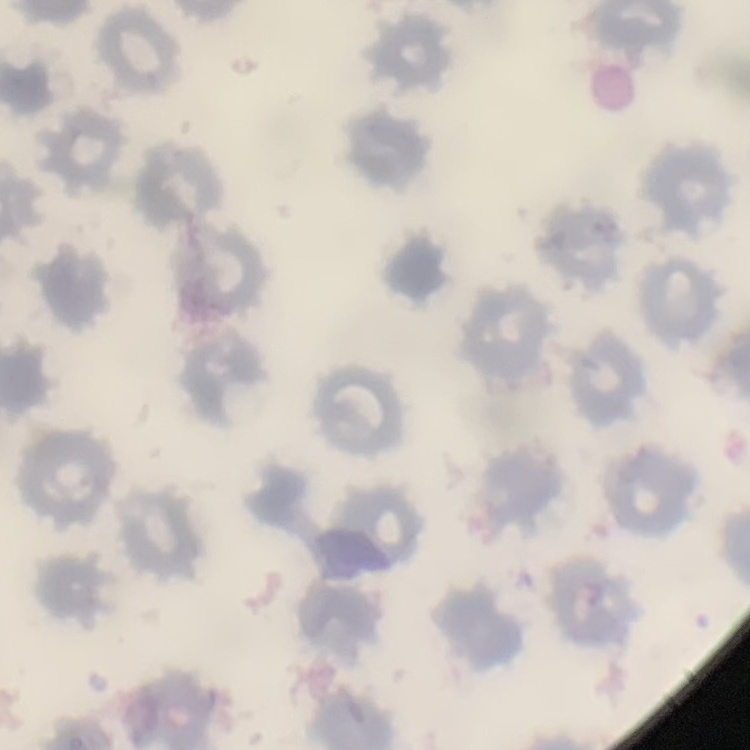

{
  "erythrocyte_morphology": "no rouleaux formation",
  "image_type": "one tile cut from a larger photomicrograph",
  "stain": "Field's or Giemsa",
  "preparation": "thin peripheral smear"
}